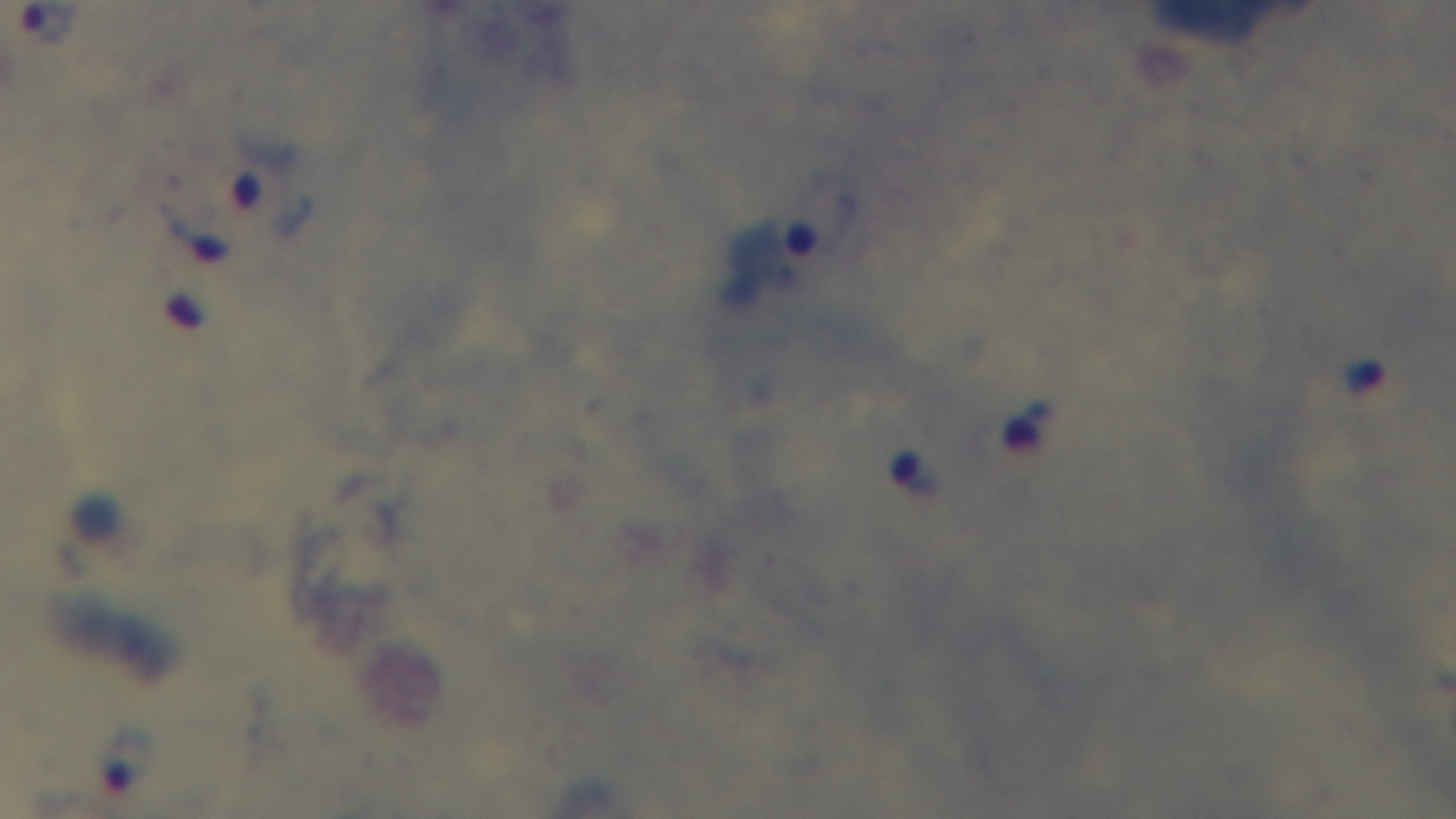

Summary:
  - Objective: 100x oil immersion
  - Field of view: one from the slide
  - Malaria status: infected
  - Stain: Giemsa
  - Preparation: thick blood film
  - Modality: light microscopy
  - Capture: mounted 4K digital camera